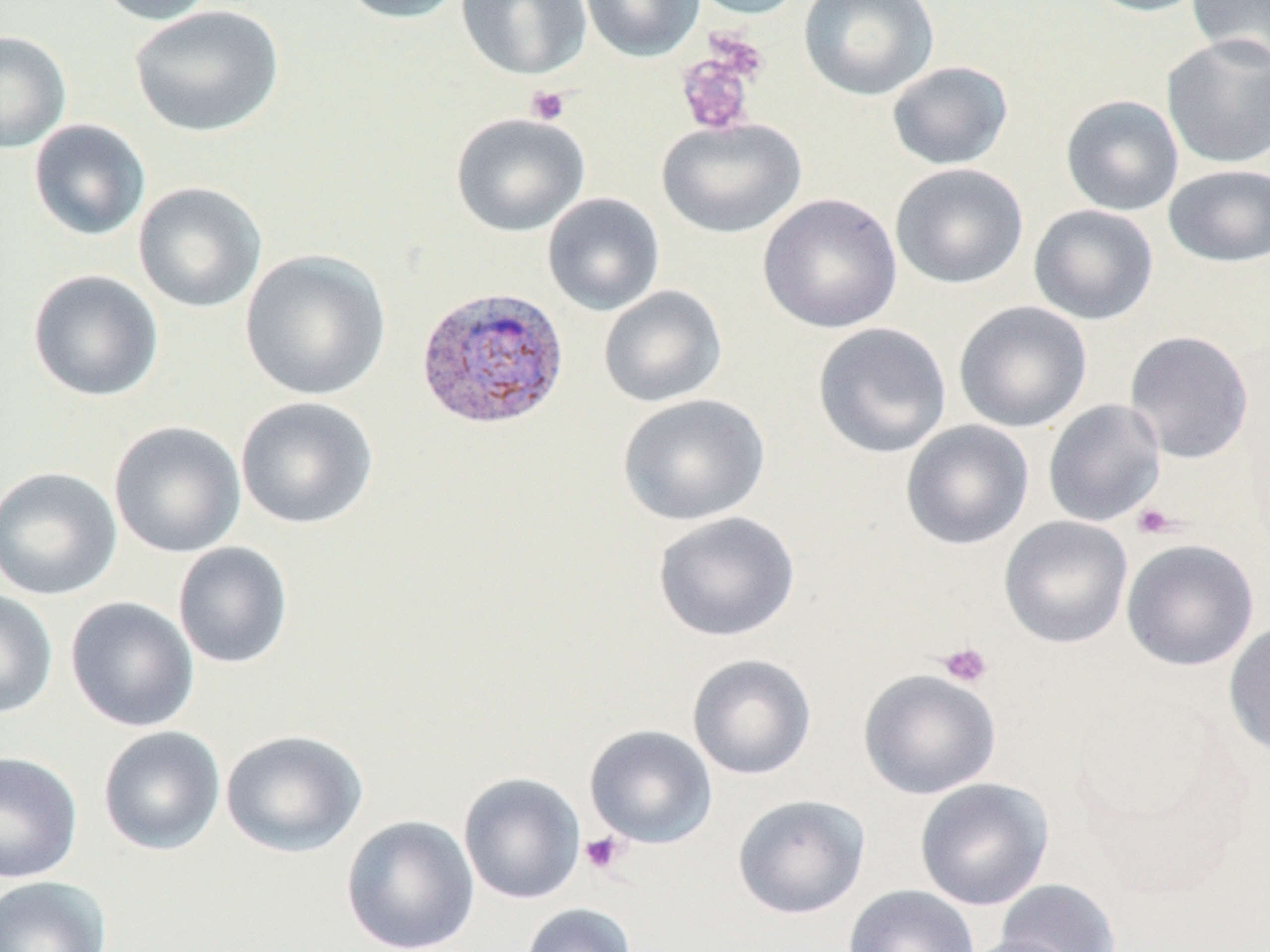

slide-level diagnosis = Plasmodium vivax
platelet locations = approximate bounding boxes as named x1/y1/x2/y2 corners in pixels: (x1=704, y1=30, x2=770, y2=84), (x1=675, y1=49, x2=758, y2=138), (x1=525, y1=85, x2=570, y2=126), (x1=1131, y1=502, x2=1180, y2=540), (x1=936, y1=641, x2=994, y2=688), (x1=579, y1=831, x2=628, y2=876)
field of view = one of a larger specimen
magnification = 1000x
preparation = thin blood film
image size = 1270×952 pixels
stain = May-Grünwald-Giemsa
uninfected red blood cell locations = approximate bounding boxes as named x1/y1/x2/y2 corners in pixels: (x1=92, y1=0, x2=219, y2=26), (x1=335, y1=0, x2=470, y2=24), (x1=456, y1=0, x2=592, y2=81), (x1=579, y1=0, x2=705, y2=62), (x1=686, y1=0, x2=808, y2=20), (x1=798, y1=0, x2=940, y2=101), (x1=1081, y1=0, x2=1213, y2=17), (x1=1186, y1=0, x2=1270, y2=69), (x1=128, y1=5, x2=284, y2=138), (x1=0, y1=31, x2=72, y2=153), (x1=1161, y1=35, x2=1270, y2=169), (x1=885, y1=60, x2=1014, y2=171), (x1=1059, y1=94, x2=1184, y2=217), (x1=450, y1=112, x2=591, y2=237), (x1=656, y1=116, x2=807, y2=239), (x1=28, y1=119, x2=151, y2=241), (x1=889, y1=162, x2=1029, y2=289), (x1=1163, y1=164, x2=1270, y2=268), (x1=132, y1=182, x2=267, y2=314), (x1=542, y1=192, x2=666, y2=317), (x1=758, y1=193, x2=902, y2=334), (x1=1028, y1=203, x2=1159, y2=326), (x1=238, y1=248, x2=392, y2=401), (x1=27, y1=269, x2=164, y2=403), (x1=598, y1=285, x2=728, y2=408), (x1=953, y1=300, x2=1093, y2=433), (x1=812, y1=322, x2=953, y2=458), (x1=1124, y1=330, x2=1254, y2=464), (x1=617, y1=392, x2=771, y2=526), (x1=235, y1=396, x2=379, y2=530), (x1=1043, y1=399, x2=1166, y2=527), (x1=108, y1=420, x2=247, y2=558), (x1=900, y1=420, x2=1035, y2=550), (x1=0, y1=466, x2=122, y2=601), (x1=652, y1=510, x2=801, y2=642), (x1=999, y1=516, x2=1133, y2=649), (x1=1121, y1=539, x2=1259, y2=671), (x1=172, y1=541, x2=294, y2=669), (x1=0, y1=588, x2=58, y2=720), (x1=65, y1=596, x2=199, y2=733), (x1=1224, y1=620, x2=1270, y2=760), (x1=687, y1=653, x2=817, y2=780), (x1=858, y1=668, x2=1001, y2=800), (x1=584, y1=724, x2=718, y2=849), (x1=97, y1=725, x2=226, y2=856), (x1=220, y1=728, x2=368, y2=858), (x1=0, y1=751, x2=83, y2=884), (x1=457, y1=772, x2=586, y2=905), (x1=914, y1=778, x2=1054, y2=911), (x1=731, y1=793, x2=870, y2=919), (x1=341, y1=815, x2=480, y2=952), (x1=0, y1=875, x2=112, y2=952), (x1=995, y1=879, x2=1122, y2=952), (x1=843, y1=884, x2=980, y2=952), (x1=520, y1=902, x2=637, y2=952), (x1=959, y1=934, x2=1083, y2=952)
modality = light microscopy
Plasmodium vivax-infected red blood cell locations = approximate bounding boxes as named x1/y1/x2/y2 corners in pixels: (x1=414, y1=284, x2=570, y2=430)